Name the parasite shown.
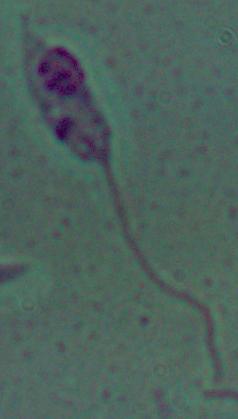

Leishmania.

Photomicrograph. Captured at 1000x magnification.